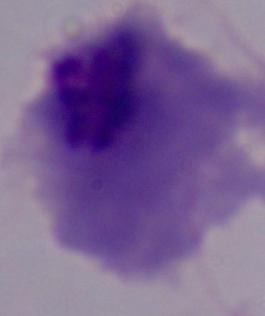

Summary:
  - Modality: micrograph
  - Magnification: 1000x
  - Identification: trichomonad